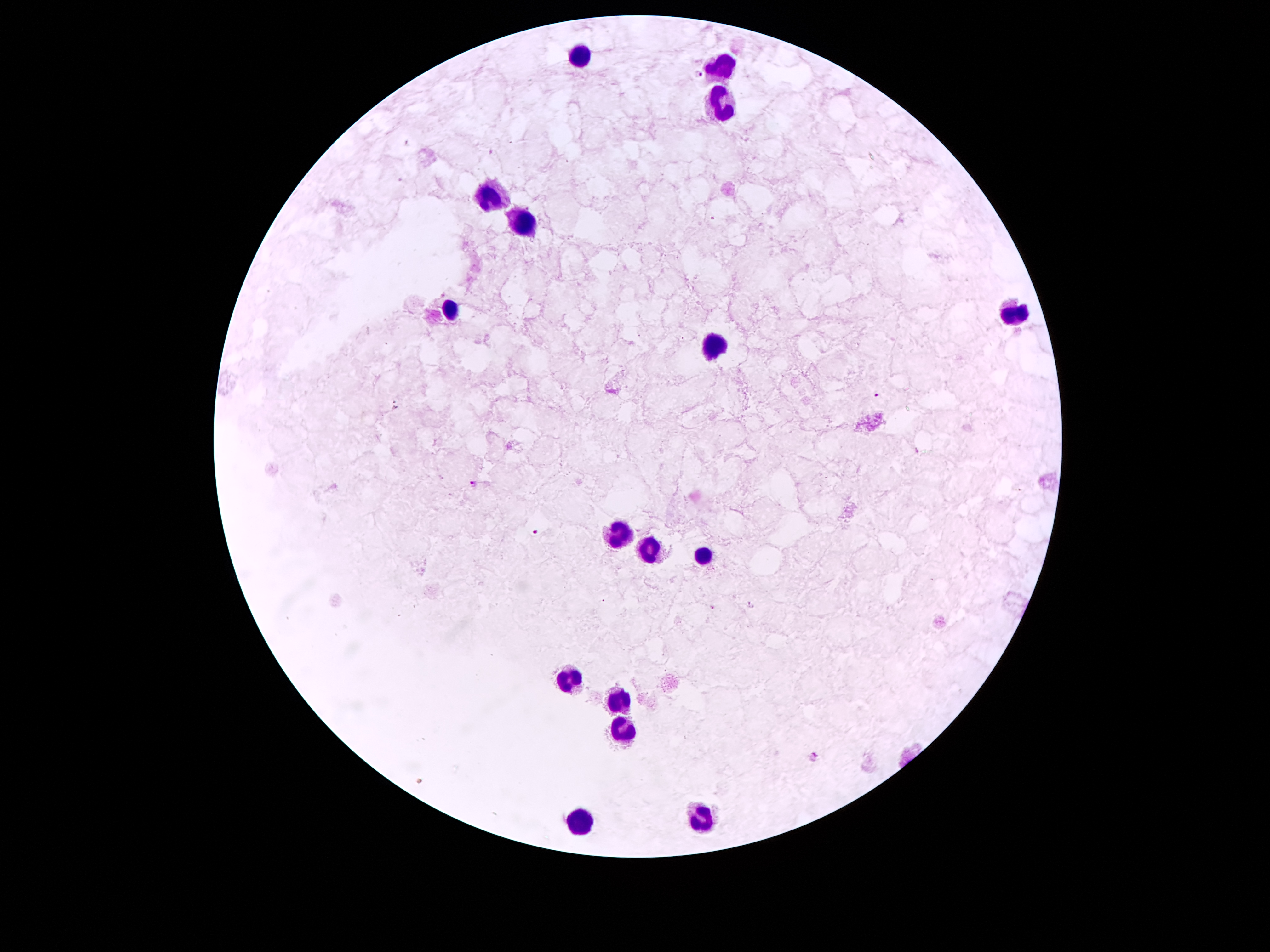
Giemsa stain. 100x magnification. Image is 1270×952 pixels. Photographed through the microscope eyepiece with a smartphone camera. Patient malaria status: infected with Plasmodium falciparum. Thick blood smear. One field from this slide.